Evaluate for parasitized red blood cells.
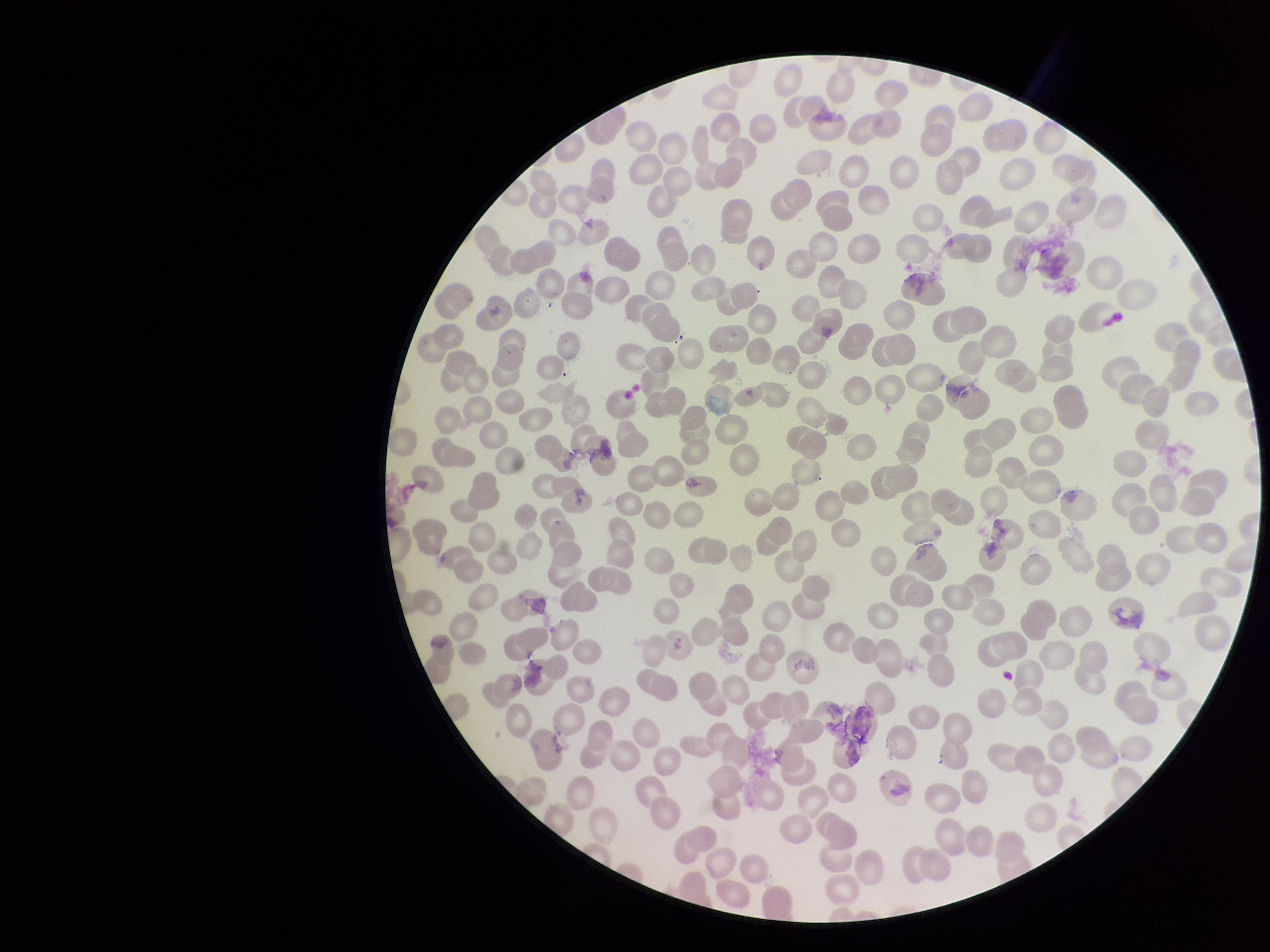
None detected.

Summary:
  - Stain: Giemsa
  - Image size: 1270×952 pixels
  - Parasitized red blood cell count: 0
  - Patient malaria status: negative
  - Preparation: thin smear
  - Capture: smartphone photograph through the microscope eyepiece
  - Field of view: single
  - Red blood cell count: 287